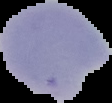
Summary:
  - Image type: segmented cell region with the area outside set to black
  - Malaria status: uninfected
  - Preparation: thin blood smear
  - Image size: 112×103 pixels